Locate every uninfected red blood cell.
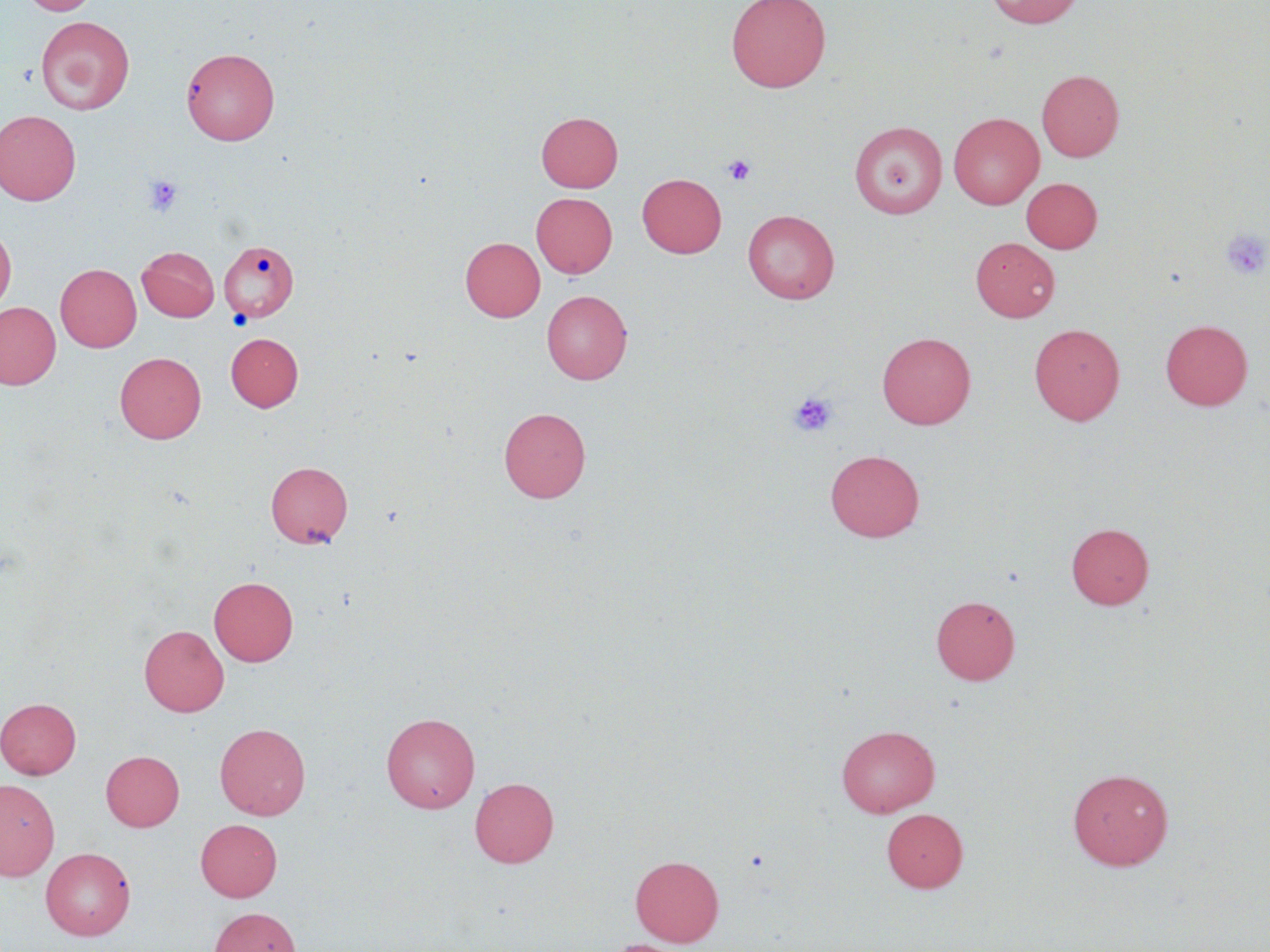
Approximate bounding boxes as (x1, y1, x2, y2) in pixels.
Uninfected red blood cells: (22, 0, 100, 16), (726, 0, 831, 92), (985, 0, 1086, 29), (36, 16, 135, 115), (181, 46, 280, 145), (1037, 69, 1124, 162), (0, 110, 81, 205), (536, 112, 623, 192), (948, 112, 1044, 209), (849, 121, 948, 218), (637, 173, 726, 258), (1021, 177, 1102, 253), (531, 192, 617, 278), (743, 210, 839, 304), (0, 225, 16, 313), (460, 237, 545, 321), (970, 237, 1059, 322), (219, 240, 299, 322), (137, 246, 220, 322), (55, 263, 141, 352), (542, 289, 632, 384), (0, 301, 61, 389), (1160, 319, 1253, 410), (1029, 323, 1125, 425), (877, 331, 975, 429), (226, 332, 304, 411), (115, 352, 206, 443), (498, 407, 590, 503), (825, 449, 924, 542), (265, 460, 353, 548), (1066, 522, 1154, 609), (209, 576, 299, 666), (931, 595, 1020, 685), (139, 624, 229, 717), (0, 698, 81, 778), (381, 712, 480, 813), (215, 723, 310, 820), (836, 725, 940, 817), (101, 750, 184, 831), (1067, 768, 1173, 870), (470, 777, 559, 867), (0, 778, 59, 880), (881, 808, 968, 892), (195, 818, 282, 901), (41, 847, 135, 940), (630, 854, 724, 946), (209, 907, 300, 952).

slide-level diagnosis = negative for blood parasites
preparation = thin blood smear
field of view = one of a larger specimen
stain = May-Grünwald-Giemsa
image size = 1270×952 pixels
platelet locations = approximate bounding boxes as (x1, y1, x2, y2) in pixels: (723, 155, 756, 186), (144, 176, 183, 216), (1221, 228, 1270, 280), (788, 391, 838, 438)
modality = optical microscopy
magnification = 1000x